Outline each Plasmodium falciparum-infected red blood cell.
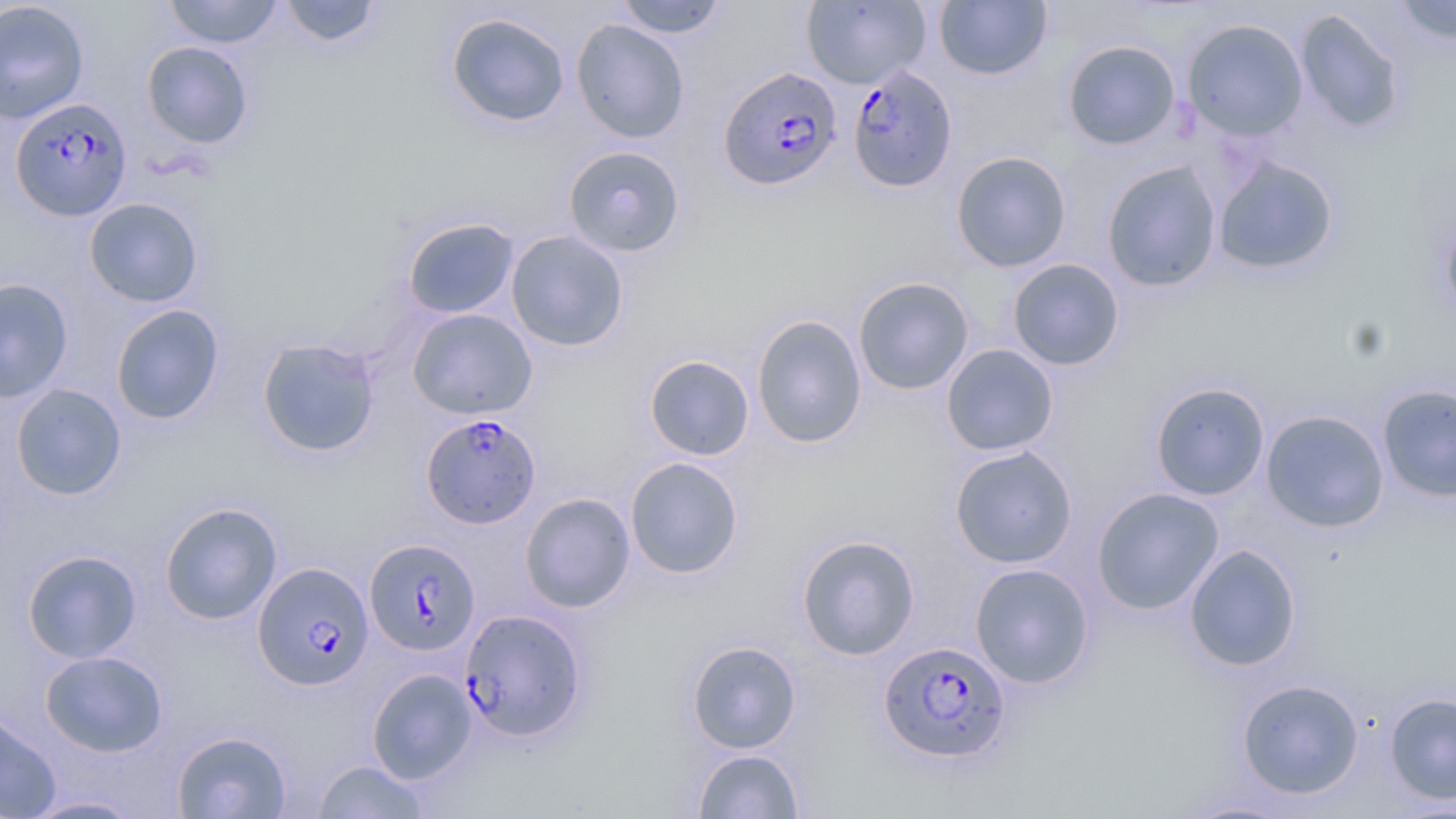

Approximate bounding boxes as [x1, y1, x2, y2] in pixels.
Plasmodium falciparum-infected red blood cells: [846, 64, 959, 193], [719, 66, 843, 192], [10, 96, 132, 221], [421, 413, 541, 529], [364, 538, 481, 656], [253, 562, 375, 690], [459, 609, 588, 744], [878, 640, 1012, 765].

slide_level_diagnosis: Plasmodium falciparum
modality: optical microscopy
stain: May-Grünwald-Giemsa
magnification: 1000x
uninfected_red_blood_cell_locations: 'approximate bounding boxes as [x1, y1, x2, y2] in pixels: [163, 0, 285, 49], [277, 0, 384, 48], [614, 0, 728, 39], [1392, 0, 1456, 45], [0, 1, 90, 124], [801, 1, 931, 89], [933, 1, 1053, 80], [1295, 9, 1406, 135], [444, 12, 571, 128], [571, 19, 690, 143], [1182, 19, 1308, 141], [1062, 39, 1181, 151], [141, 41, 254, 149], [562, 145, 686, 258], [951, 150, 1072, 272], [1212, 155, 1340, 277], [1102, 160, 1222, 293], [84, 197, 204, 307], [1439, 209, 1456, 325], [402, 216, 520, 319], [506, 230, 629, 351], [1007, 258, 1125, 371], [853, 276, 975, 395], [0, 277, 74, 404], [110, 304, 225, 426], [407, 308, 538, 420], [751, 314, 868, 449], [257, 337, 381, 457], [941, 344, 1059, 456], [644, 354, 755, 460], [1150, 381, 1270, 501], [10, 383, 127, 501], [1377, 383, 1456, 503], [1261, 409, 1390, 532], [949, 445, 1078, 569], [625, 457, 744, 579], [1092, 486, 1225, 615], [519, 492, 636, 613], [159, 502, 283, 625], [796, 534, 921, 661], [1184, 543, 1302, 672], [22, 549, 143, 663], [969, 563, 1095, 689], [686, 640, 801, 754], [40, 650, 169, 757], [367, 668, 478, 785], [1236, 679, 1365, 799], [1384, 692, 1456, 805], [0, 708, 62, 819], [172, 730, 292, 818], [692, 748, 805, 818], [313, 760, 430, 818], [19, 795, 148, 817], [1175, 797, 1300, 818]'
image_size: 1456×819 pixels
field_of_view: one of a larger specimen
preparation: thin blood smear